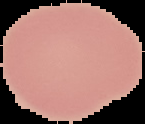

preparation = thin blood smear
image type = cell region segmented out of the field of view; surrounding area masked to black
result = no Plasmodium parasites seen
image size = 145×124 pixels